Give the position of every malaria parasite.
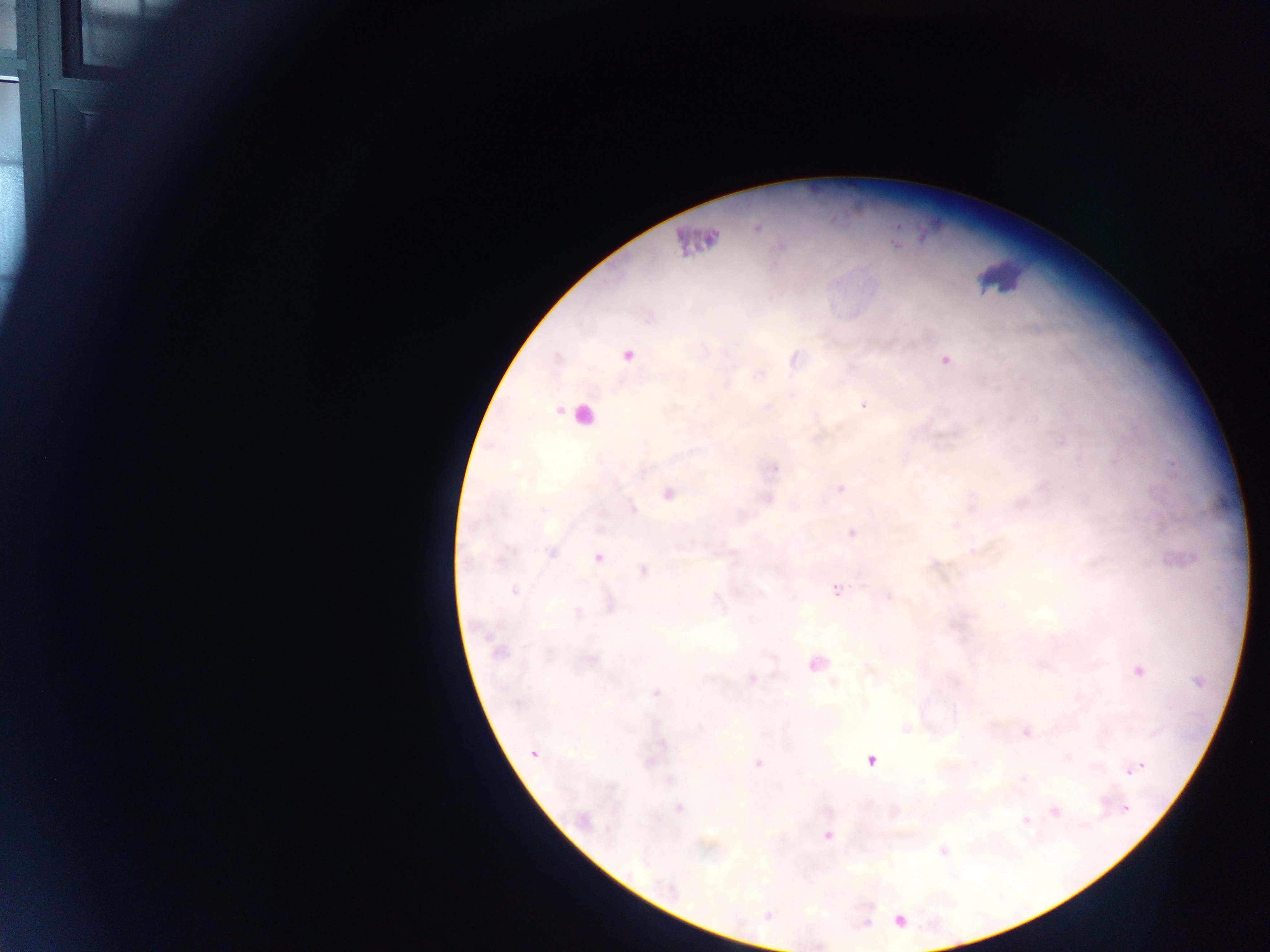
Approximate centers as x y in pixels.
Malaria parasites: 758 228; 628 355; 945 360; 768 406; 863 406; 1062 440; 774 468; 839 489; 669 494; 1086 500; 633 508; 972 508; 852 533; 974 552; 552 553; 598 557; 642 571; 836 589; 514 591; 889 596; 577 613; 498 653; 1139 671; 751 678; 656 692; 1027 732; 664 745; 533 753; 870 761; 757 763; 1134 769; 1023 779; 669 780; 679 809; 1126 809; 1054 811; 582 820; 1026 821; 608 831; 827 835; 671 888; 900 921.

Leukocyte locations (subset; some below the resolvable size): 697 246; 998 274; 577 415. Image is 1270×952 pixels. Single field of view. Photographed through a microscope with a mobile-phone camera. Collected in Ghana. Thick blood smear.